Locate every blood parasite and identify its species.
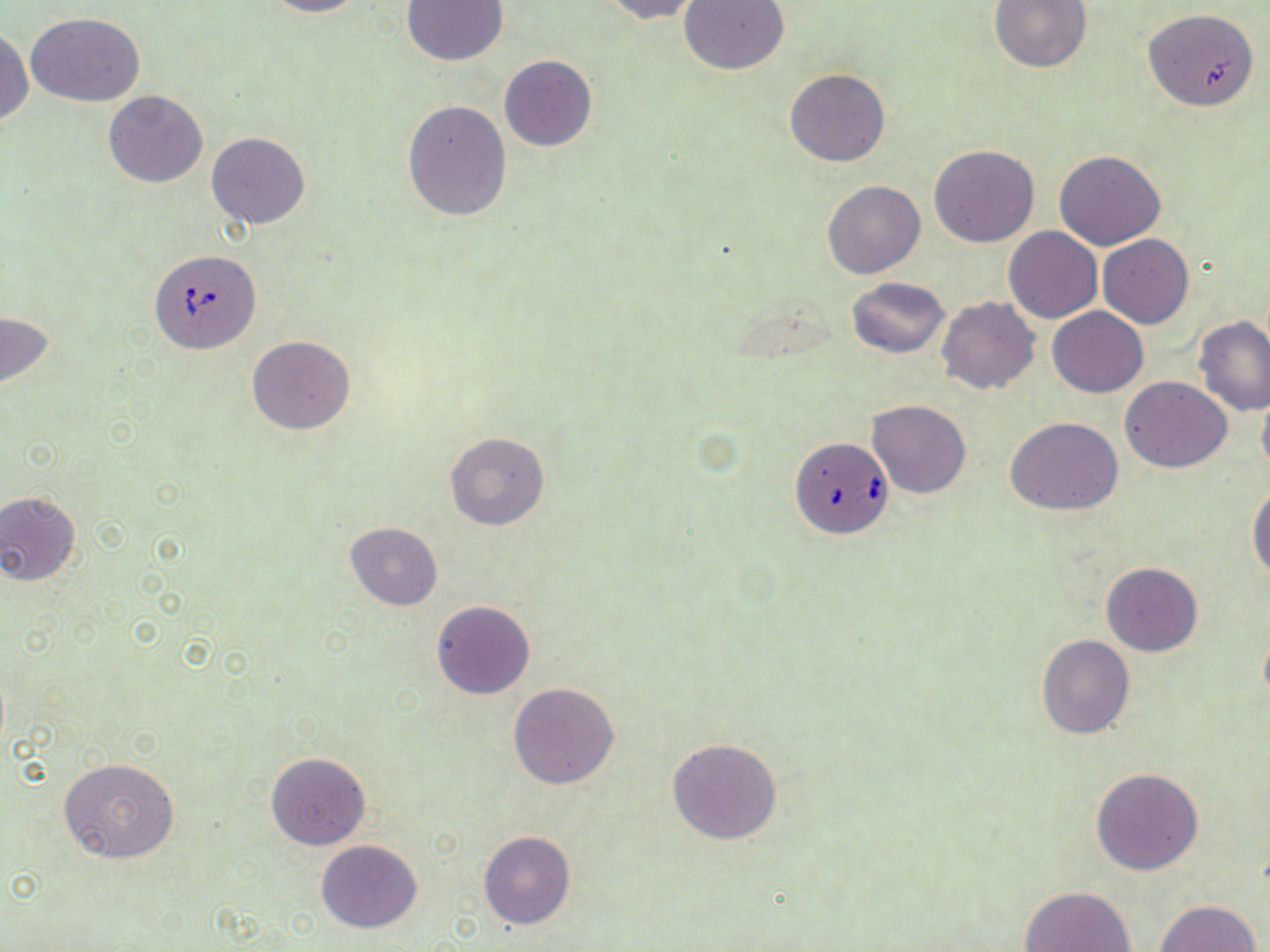
Approximate bounding boxes as (x1,y1)-(x2,y2) corner pairs in pixels.
Babesia divergens-infected red blood cells: (150,250)-(261,353), (791,435)-(895,539).
No Plasmodium falciparum, Plasmodium ovale, Plasmodium malariae, Plasmodium vivax, or Trypanosoma brucei observed.

slide-level diagnosis = Babesia divergens
stain = May-Grünwald-Giemsa
preparation = thin blood smear
modality = light microscopy
uninfected red blood cell locations = approximate bounding boxes as (x1,y1)-(x2,y2) corner pairs in pixels: (258,0)-(365,18), (595,0)-(703,23), (679,0)-(789,75), (989,0)-(1093,73), (400,1)-(508,68), (1144,11)-(1260,116), (27,13)-(146,105), (0,28)-(32,127), (499,55)-(597,151), (785,69)-(889,167), (103,91)-(208,188), (402,100)-(512,221), (207,131)-(310,229), (928,144)-(1040,248), (1053,152)-(1165,251), (821,180)-(926,280), (1004,227)-(1102,323), (1098,235)-(1193,329), (846,276)-(950,358), (937,296)-(1040,395), (1047,307)-(1148,397), (0,312)-(55,393), (1194,317)-(1270,416), (247,334)-(357,435), (1120,376)-(1232,473), (1256,387)-(1270,481), (866,400)-(970,497), (1006,418)-(1123,516), (444,431)-(550,531), (1248,484)-(1270,582), (0,492)-(83,586), (344,522)-(442,610), (1100,562)-(1202,656), (431,600)-(535,699), (1036,636)-(1133,738), (507,682)-(618,789), (667,738)-(782,844), (265,752)-(371,851), (58,759)-(180,865), (1090,768)-(1204,875), (478,831)-(576,930), (316,840)-(421,932), (1018,886)-(1135,952), (1154,900)-(1262,952)
image size = 1270×952 pixels
field of view = one of a larger specimen
magnification = 1000x